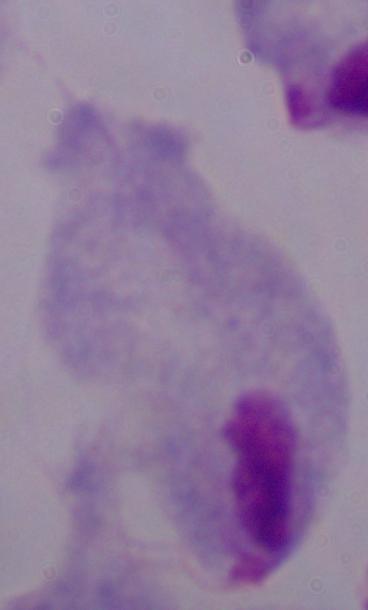
magnification = 1000x
modality = micrograph
identification = trichomonad